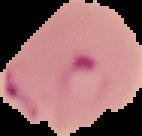

malaria status = parasitized
image type = segmented cell region with the area outside set to black
image size = 142×136 pixels
preparation = thin blood film